Name the parasite shown.
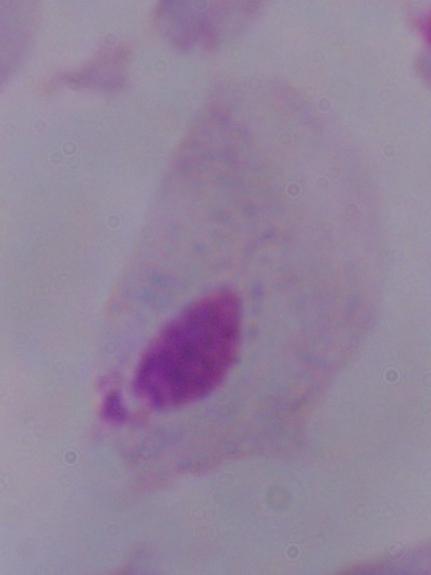
A trichomonad.

magnification = 1000x
modality = photomicrograph